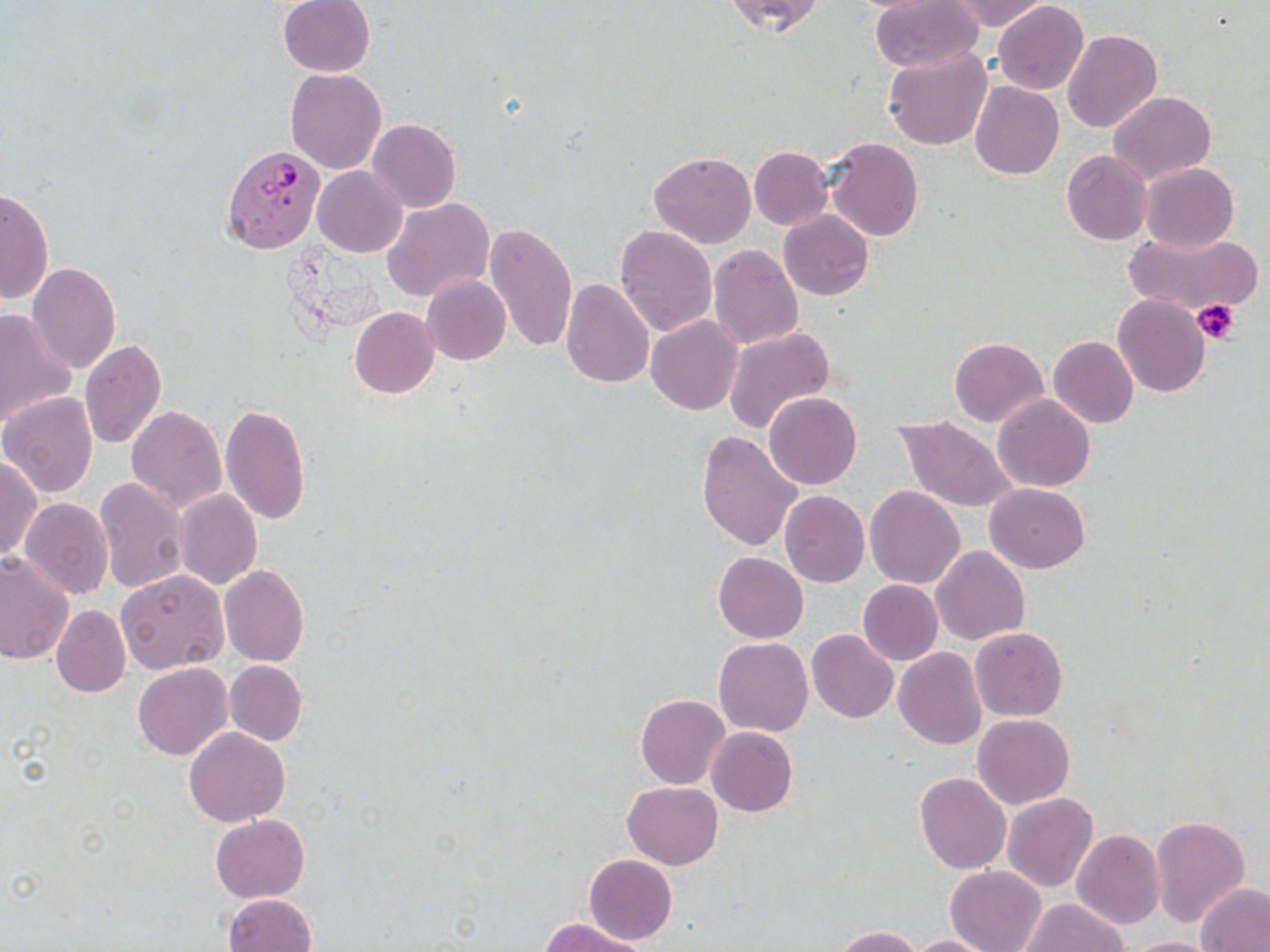

Approximate bounding boxes as [x1, y1, x2, y2] in pixels. Plasmodium falciparum-infected red blood cell locations: [222, 145, 327, 255]. Uninfected red blood cell locations: [277, 0, 376, 77], [723, 0, 825, 36], [868, 0, 986, 73], [941, 0, 1052, 32], [992, 1, 1089, 96], [1061, 29, 1162, 133], [883, 48, 992, 152], [285, 68, 388, 174], [971, 82, 1063, 179], [1107, 90, 1215, 184], [368, 118, 461, 212], [823, 138, 924, 241], [749, 145, 833, 231], [1061, 150, 1153, 246], [648, 152, 757, 249], [1139, 163, 1239, 253], [313, 166, 407, 257], [0, 186, 53, 306], [382, 197, 495, 305], [778, 211, 873, 301], [485, 222, 578, 356], [612, 224, 717, 338], [1123, 230, 1263, 319], [708, 245, 802, 349], [26, 262, 121, 375], [421, 274, 510, 367], [561, 278, 654, 390], [1112, 296, 1211, 398], [0, 307, 79, 434], [348, 307, 439, 398], [645, 316, 742, 416], [723, 327, 836, 434], [1048, 336, 1138, 429], [949, 337, 1047, 427], [79, 339, 167, 450], [1, 392, 97, 497], [765, 392, 862, 489], [992, 395, 1096, 492], [730, 401, 834, 529], [219, 404, 312, 526], [125, 405, 227, 513], [896, 416, 1018, 513], [696, 431, 804, 551], [0, 453, 41, 564], [93, 477, 190, 594], [985, 484, 1090, 573], [865, 485, 964, 589], [173, 489, 262, 590], [779, 491, 870, 587], [20, 498, 113, 599], [931, 545, 1029, 645], [712, 552, 808, 644], [0, 553, 73, 667], [219, 565, 309, 667], [116, 570, 227, 675], [857, 579, 942, 666], [50, 603, 131, 698], [970, 627, 1067, 722], [806, 629, 899, 724], [714, 637, 813, 737], [893, 647, 986, 750], [224, 660, 307, 746], [132, 661, 233, 760], [635, 694, 731, 789], [972, 713, 1075, 808], [706, 726, 797, 817], [184, 727, 290, 827], [914, 771, 1011, 874], [622, 782, 722, 870], [1002, 792, 1098, 892], [211, 814, 309, 902], [1149, 814, 1251, 931], [1071, 829, 1165, 930], [584, 854, 678, 945], [944, 865, 1046, 952], [1196, 882, 1270, 951], [224, 892, 317, 952], [1021, 898, 1126, 952], [538, 917, 651, 952], [832, 926, 924, 952], [903, 935, 1002, 952], [1118, 935, 1225, 951]. Platelet locations: [1192, 298, 1239, 345]. Slide-level diagnosis: Plasmodium falciparum. Thin blood film. Captured at 1000x magnification. May-Grünwald-Giemsa stain. Image is 1270×952 pixels. Single field of view. Light microscopy.